Outline each P. falciparum parasite and classify it by life-cycle stage.
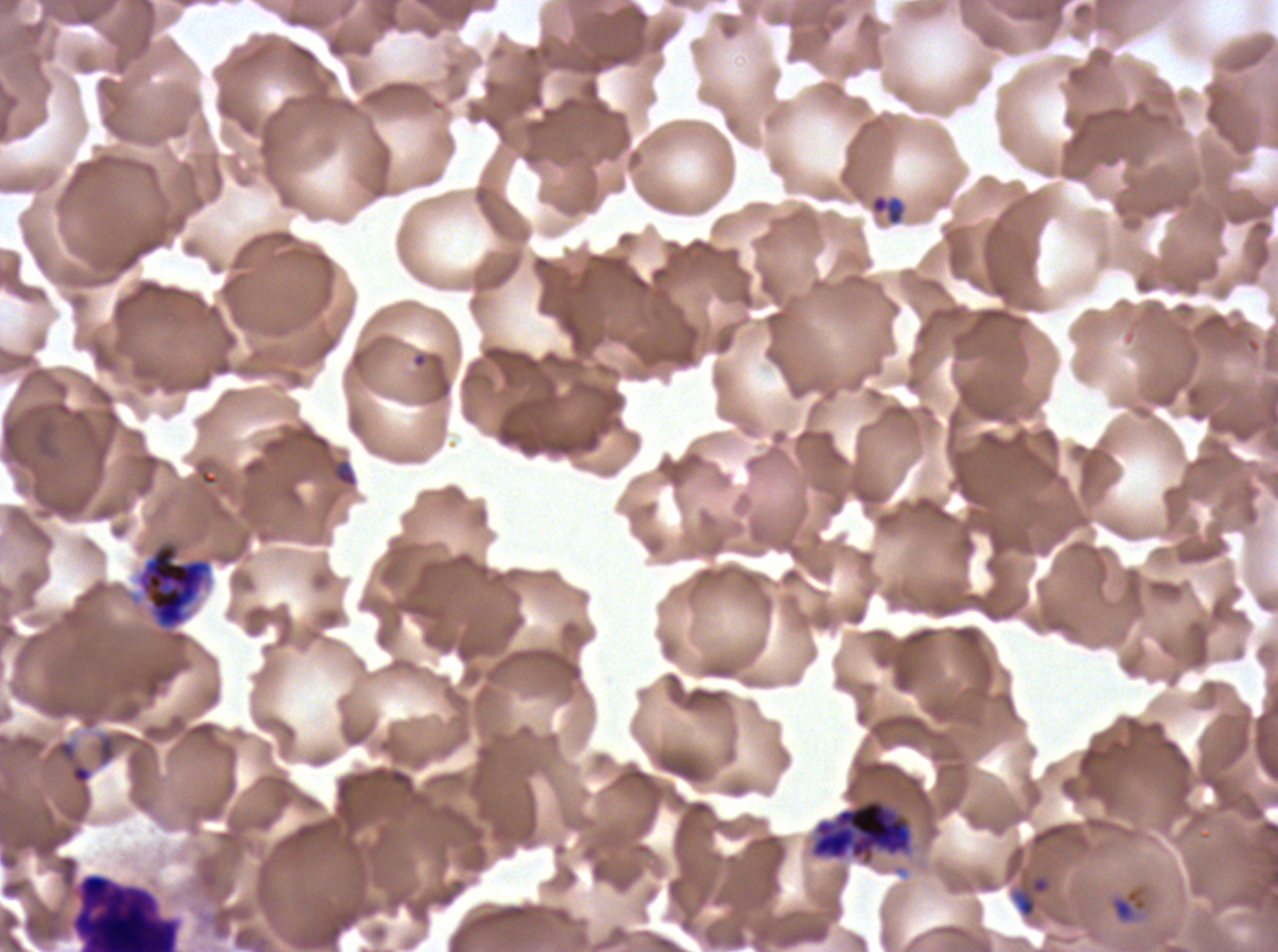
Approximate bounding boxes as [x1, y1, x2, y2] in pixels.
Rings: [53, 738, 94, 787].
Late-ring/early-trophozoite forms: [870, 194, 903, 225], [1108, 884, 1149, 925].
Segmenters: [137, 543, 211, 629], [809, 797, 914, 865].
No mid trophozoites, late trophozoites, early schizonts, late schizonts, or gametocytes observed.

Leukocyte locations: [70, 873, 180, 951]. Debris locations: [1012, 874, 1051, 919]. Thin blood smear. Ex-vivo P. falciparum culture from a patient in The Gambia, grown for 24 to 48 hours. One sub-image of a larger composite. Life-cycle stages observed: ring, late-ring/early-trophozoite, segmenter. Image is 1278×952 pixels. Giemsa stain.